Name the parasite shown.
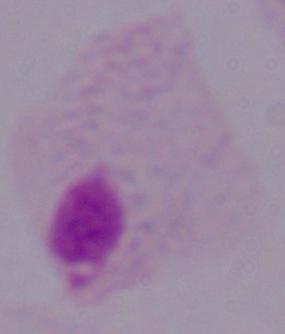
A trichomonad.

magnification: 1000x
modality: photomicrograph